Describe the morphology of the red blood cells.
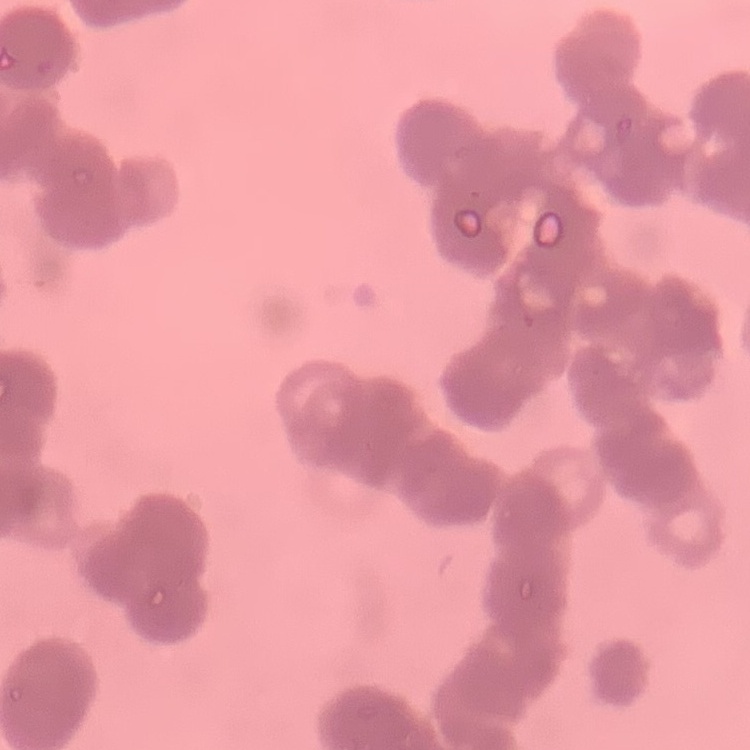

Rouleaux formation.

Summary:
  - Stain: Field's or Giemsa
  - Image type: one tile cut from a larger photomicrograph
  - Preparation: thin blood film